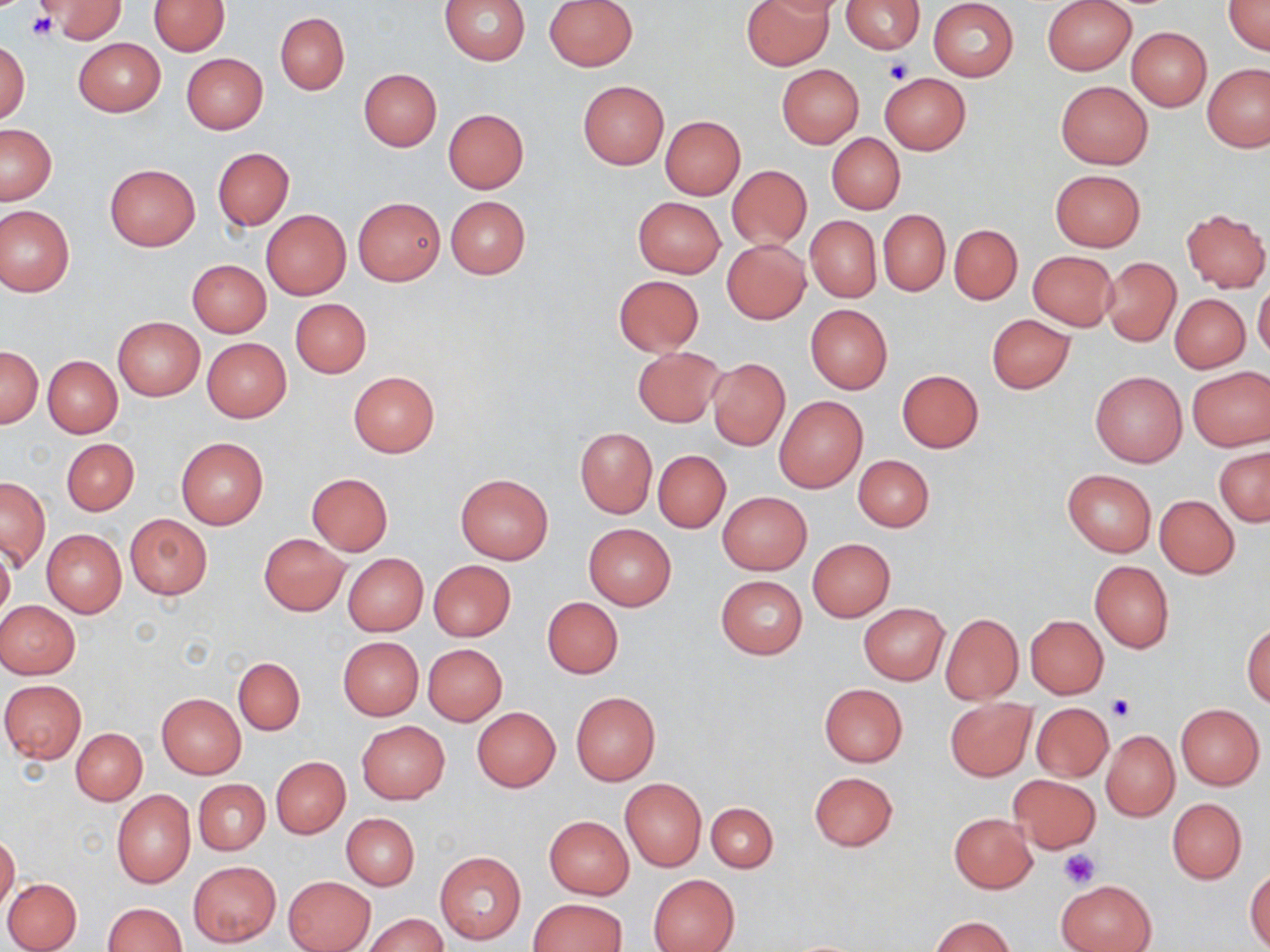

slide-level diagnosis = negative for blood parasites
field of view = single
image size = 1270×952 pixels
platelet locations = approximate bounding boxes as [x1, y1, x2, y2] in pixels: [28, 13, 57, 41], [883, 58, 914, 84], [1108, 695, 1136, 723], [1058, 850, 1101, 888]
preparation = thin blood smear
uninfected red blood cell locations = approximate bounding boxes as [x1, y1, x2, y2] in pixels: [41, 0, 124, 41], [148, 0, 228, 55], [440, 0, 531, 64], [545, 0, 637, 70], [741, 0, 833, 70], [755, 0, 845, 18], [1042, 0, 1136, 75], [1223, 0, 1270, 56], [841, 1, 925, 53], [928, 1, 1018, 81], [275, 12, 349, 94], [1126, 27, 1212, 110], [74, 38, 165, 116], [0, 40, 30, 125], [182, 53, 267, 133], [1202, 62, 1270, 151], [777, 65, 864, 147], [359, 68, 442, 150], [879, 73, 970, 154], [578, 81, 668, 169], [1055, 81, 1153, 169], [443, 108, 528, 193], [659, 115, 745, 198], [0, 124, 57, 205], [827, 133, 905, 215], [213, 148, 294, 230], [104, 163, 201, 252], [727, 165, 812, 251], [1050, 169, 1145, 251], [353, 196, 444, 285], [445, 196, 531, 279], [633, 197, 725, 277], [0, 206, 74, 296], [1182, 209, 1270, 293], [261, 210, 351, 298], [878, 210, 950, 295], [805, 215, 881, 303], [948, 224, 1022, 305], [722, 240, 810, 323], [1027, 250, 1118, 330], [1103, 258, 1180, 346], [187, 259, 271, 337], [613, 275, 705, 356], [1253, 281, 1270, 362], [1170, 294, 1249, 373], [290, 298, 371, 378], [804, 304, 892, 395], [986, 314, 1075, 393], [112, 316, 205, 401], [202, 338, 291, 421], [0, 345, 42, 428], [631, 346, 724, 426], [44, 355, 122, 438], [707, 357, 790, 451], [1187, 366, 1270, 451], [1090, 369, 1188, 467], [897, 370, 984, 453], [348, 371, 439, 456], [774, 396, 868, 493], [574, 428, 656, 517], [177, 437, 268, 529], [61, 438, 137, 515], [1215, 445, 1270, 526], [654, 450, 731, 533], [854, 455, 933, 532], [1062, 468, 1156, 556], [306, 472, 393, 556], [456, 472, 554, 564], [1, 477, 50, 569], [717, 491, 812, 575], [1155, 495, 1239, 578], [125, 514, 213, 600], [583, 524, 676, 610], [42, 529, 126, 616], [258, 533, 348, 614], [808, 538, 896, 621], [0, 547, 15, 623], [342, 553, 428, 635], [429, 559, 517, 641], [1089, 561, 1174, 652], [717, 576, 807, 659], [542, 597, 623, 678], [0, 600, 80, 677], [859, 602, 950, 685], [939, 613, 1023, 704], [1026, 615, 1108, 698], [1243, 622, 1270, 707], [338, 637, 424, 720], [423, 643, 507, 725], [233, 657, 304, 735], [1, 679, 87, 763], [819, 684, 907, 767], [571, 692, 660, 785], [157, 693, 246, 777], [944, 698, 1035, 781], [1176, 703, 1265, 789], [1031, 704, 1114, 782], [472, 707, 561, 792], [357, 721, 450, 803], [71, 728, 146, 804], [1102, 730, 1179, 821], [272, 757, 350, 838], [809, 772, 898, 851], [1007, 774, 1100, 853], [620, 778, 707, 871], [194, 779, 269, 854], [113, 790, 195, 888], [1167, 798, 1247, 883], [706, 802, 777, 873], [342, 813, 419, 889], [948, 813, 1037, 894], [544, 815, 634, 898], [0, 832, 20, 910], [434, 851, 526, 945], [188, 861, 281, 946], [1246, 869, 1270, 951], [648, 874, 740, 952], [283, 875, 375, 952], [3, 878, 81, 952], [1058, 879, 1153, 951], [529, 898, 626, 951], [102, 902, 187, 952], [365, 913, 447, 952], [930, 916, 1015, 952]
stain = May-Grünwald-Giemsa
magnification = 1000x
modality = light microscopy